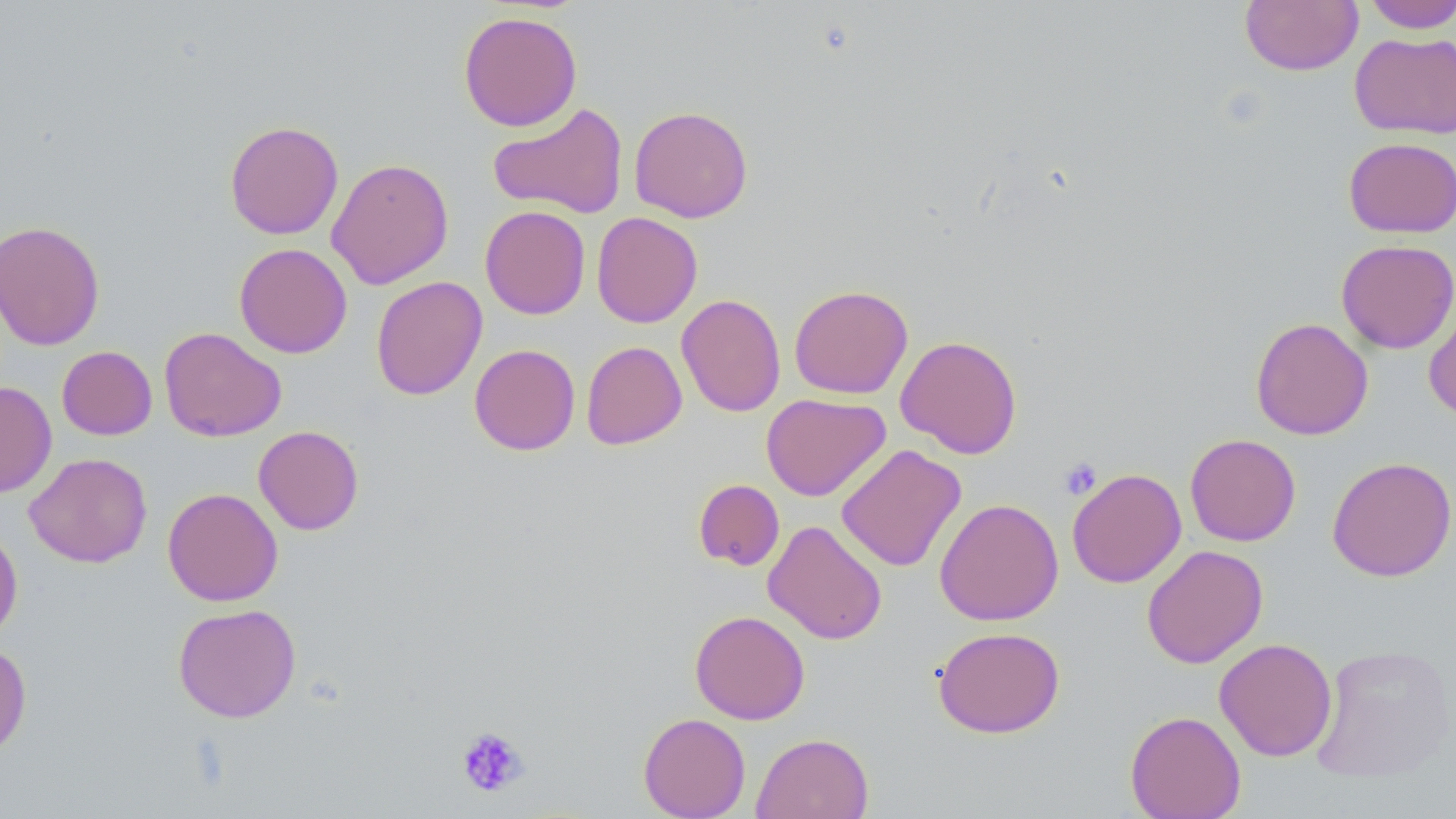

slide-level diagnosis = no evidence of blood parasites
modality = optical microscopy
magnification = 1000x
preparation = thin blood film
stain = May-Grünwald-Giemsa
image size = 1456×819 pixels
platelet locations = approximate bounding boxes as (x1, y1, x2, y2) in pixels: (1059, 457, 1103, 501), (455, 725, 530, 798)
field of view = single
uninfected red blood cell locations = approximate bounding boxes as (x1, y1, x2, y2) in pixels: (1240, 0, 1362, 75), (1360, 0, 1456, 33), (458, 10, 582, 131), (1350, 32, 1456, 140), (487, 103, 629, 219), (628, 105, 754, 223), (225, 120, 343, 240), (1343, 137, 1456, 238), (326, 157, 454, 289), (480, 205, 591, 319), (591, 212, 703, 328), (0, 220, 105, 350), (1335, 239, 1456, 353), (234, 242, 352, 358), (370, 276, 487, 400), (789, 284, 913, 399), (676, 293, 786, 417), (1423, 293, 1456, 423), (1250, 317, 1373, 440), (159, 327, 287, 442), (895, 335, 1022, 458), (581, 341, 687, 450), (469, 343, 580, 456), (57, 346, 157, 440), (0, 381, 57, 497), (761, 393, 890, 501), (253, 425, 364, 535), (1185, 433, 1301, 546), (836, 444, 966, 572), (24, 452, 152, 568), (1327, 456, 1456, 582), (1066, 468, 1186, 588), (693, 479, 784, 571), (162, 487, 283, 606), (935, 498, 1064, 626), (763, 520, 888, 644), (0, 524, 23, 642), (1141, 545, 1268, 669), (172, 603, 301, 723), (689, 610, 810, 724), (932, 626, 1066, 738), (1214, 638, 1337, 762), (0, 641, 32, 760), (1310, 643, 1455, 783), (1124, 710, 1247, 819), (638, 712, 751, 819), (752, 732, 873, 819)